Give the extent of all Plasmodium falciparum-infected red blood cells.
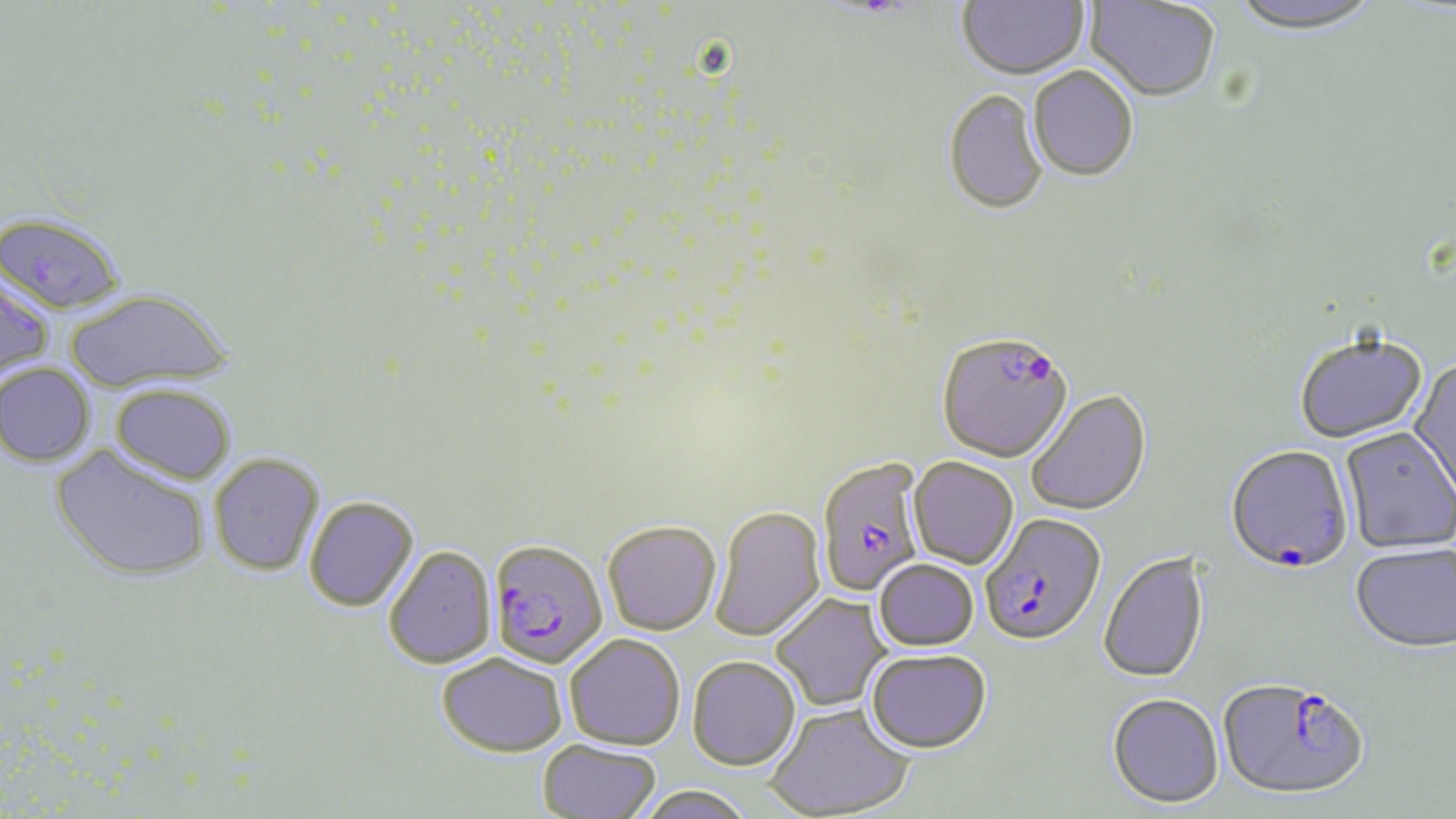
Approximate bounding boxes as named x1/y1/x2/y2 corners in pixels.
Plasmodium falciparum-infected red blood cells: (x1=0, y1=213, x2=126, y2=316), (x1=0, y1=270, x2=55, y2=383), (x1=937, y1=336, x2=1074, y2=465), (x1=1224, y1=447, x2=1354, y2=578), (x1=816, y1=459, x2=926, y2=597), (x1=978, y1=518, x2=1105, y2=650), (x1=488, y1=540, x2=607, y2=669), (x1=1217, y1=681, x2=1370, y2=805).

slide_level_diagnosis: Plasmodium falciparum
magnification: 1000x
preparation: thin blood film
field_of_view: single
modality: optical microscopy
image_size: 1456×819 pixels
stain: May-Grünwald-Giemsa
uninfected_red_blood_cell_locations: 'approximate bounding boxes as named x1/y1/x2/y2 corners in pixels: (x1=957, y1=0, x2=1088, y2=82), (x1=1227, y1=0, x2=1383, y2=39), (x1=1085, y1=1, x2=1220, y2=104), (x1=1028, y1=68, x2=1138, y2=184), (x1=943, y1=91, x2=1048, y2=217), (x1=65, y1=289, x2=233, y2=394), (x1=1294, y1=336, x2=1427, y2=445), (x1=1408, y1=359, x2=1456, y2=504), (x1=0, y1=362, x2=96, y2=468), (x1=111, y1=384, x2=237, y2=485), (x1=1026, y1=391, x2=1152, y2=517), (x1=1340, y1=429, x2=1455, y2=555), (x1=50, y1=445, x2=210, y2=582), (x1=209, y1=453, x2=324, y2=576), (x1=908, y1=458, x2=1018, y2=570), (x1=304, y1=496, x2=419, y2=611), (x1=711, y1=507, x2=826, y2=643), (x1=602, y1=523, x2=721, y2=636), (x1=384, y1=545, x2=497, y2=669), (x1=1350, y1=546, x2=1456, y2=656), (x1=1099, y1=552, x2=1210, y2=685), (x1=874, y1=560, x2=979, y2=652), (x1=771, y1=594, x2=891, y2=712), (x1=565, y1=634, x2=685, y2=750), (x1=865, y1=651, x2=992, y2=755), (x1=437, y1=652, x2=568, y2=756), (x1=687, y1=657, x2=800, y2=773), (x1=1107, y1=695, x2=1224, y2=810), (x1=766, y1=705, x2=914, y2=819), (x1=538, y1=739, x2=661, y2=818), (x1=634, y1=786, x2=755, y2=819)'